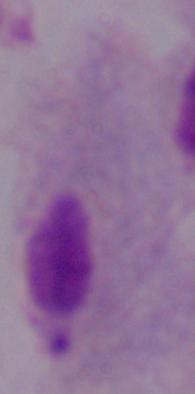

Micrograph. A trichomonad is shown. Captured at 1000x magnification.